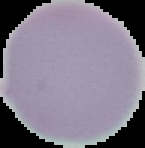
Result: no Plasmodium parasites seen. Segmented cell region on a black background. Image is 145×148 pixels. From a thin blood film.